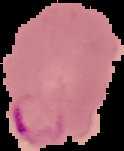

Summary:
  - Image size: 124×151 pixels
  - Image type: cell region segmented out of the field of view; surrounding area masked to black
  - Result: Plasmodium parasites identified
  - Preparation: thin blood film